Name the blood parasite species.
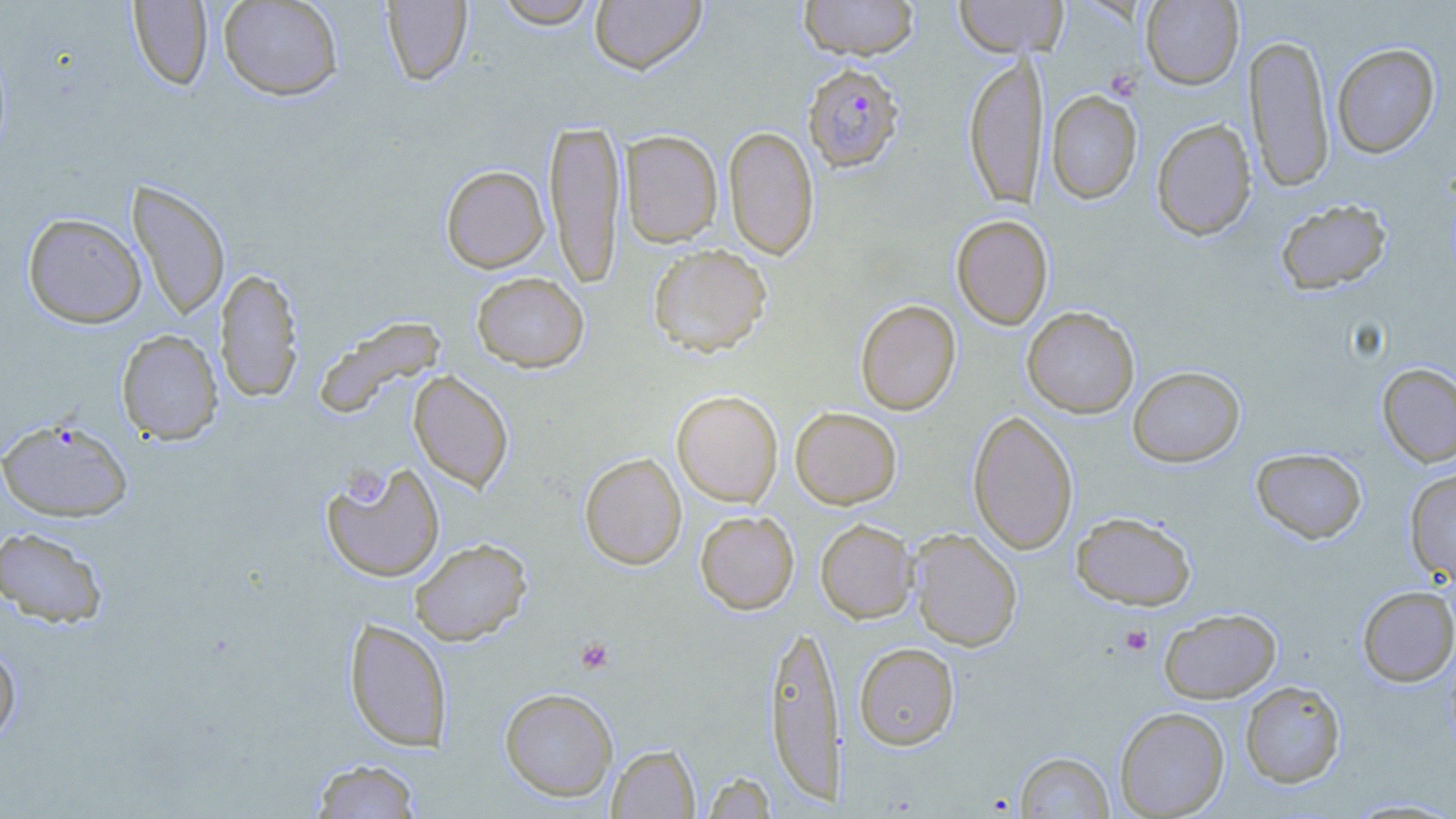

Plasmodium falciparum.

Approximate bounding boxes as (x1,y1)-(x2,y2) corner pairs in pixels. Plasmodium falciparum-infected red blood cell locations: (803,62)-(904,172). Uninfected red blood cell locations: (218,0)-(344,101), (491,0)-(601,28), (589,0)-(707,74), (798,0)-(920,60), (953,0)-(1068,58), (127,1)-(213,90), (380,1)-(472,85), (1141,1)-(1243,89), (1244,32)-(1334,193), (1332,42)-(1440,158), (962,52)-(1047,208), (1046,90)-(1142,204), (544,118)-(625,288), (1151,118)-(1257,240), (724,125)-(819,260), (619,129)-(723,247), (441,164)-(549,273), (127,179)-(231,321), (1274,198)-(1393,295), (23,212)-(146,328), (951,214)-(1053,330), (647,243)-(772,357), (215,267)-(303,404), (471,271)-(589,373), (855,299)-(961,415), (1022,306)-(1139,418), (313,315)-(447,419), (116,329)-(223,446), (1376,363)-(1456,467), (1128,365)-(1245,467), (408,370)-(514,492), (671,390)-(783,507), (790,406)-(902,508), (968,410)-(1078,554), (0,418)-(134,522), (1251,447)-(1367,544), (579,453)-(687,569), (321,460)-(446,582), (1405,469)-(1456,584), (695,510)-(799,614), (1071,511)-(1196,610), (815,518)-(919,623), (0,526)-(109,628), (908,529)-(1023,651), (409,538)-(532,646), (1357,586)-(1456,686), (1159,608)-(1281,703), (344,618)-(453,752), (764,619)-(846,806), (0,639)-(21,746), (854,642)-(960,749), (1240,680)-(1346,788), (499,687)-(618,801), (1114,706)-(1230,818), (607,744)-(700,818), (1015,751)-(1114,818), (309,759)-(424,818), (700,770)-(777,818), (1344,797)-(1456,818). Platelet locations: (345,467)-(383,505), (1120,625)-(1154,655), (576,637)-(615,673). Optical microscopy. One field of a larger specimen. Thin blood film. Image is 1456×819 pixels. May-Grünwald-Giemsa stain. 1000x magnification.